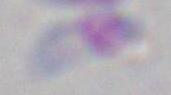

identification: Toxoplasma gondii
magnification: 1000x
modality: micrograph